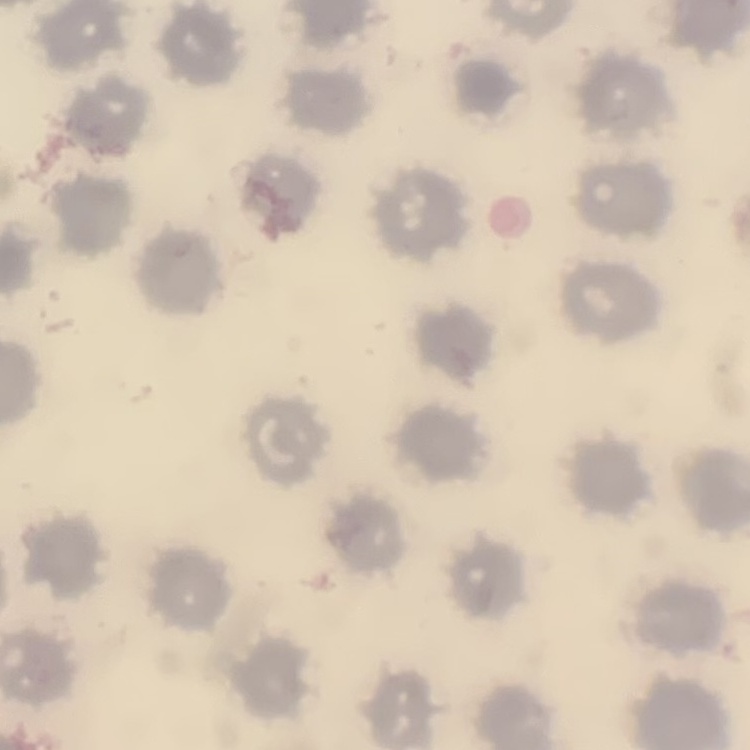

The red blood cells exhibit no rouleaux formation. Thin peripheral smear. Square crop of a larger photomicrograph. Field's or Giemsa stain.